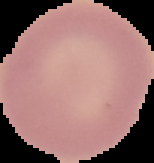

preparation = thin blood smear
malaria status = uninfected
image size = 154×163 pixels
image type = cell region segmented out of the field of view; surrounding area masked to black